Classify this cell by malaria status.
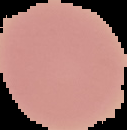
It is uninfected.

From a thin blood film. Cell region segmented out of the field of view; the surrounding area is masked to black. Image is 127×130 pixels.